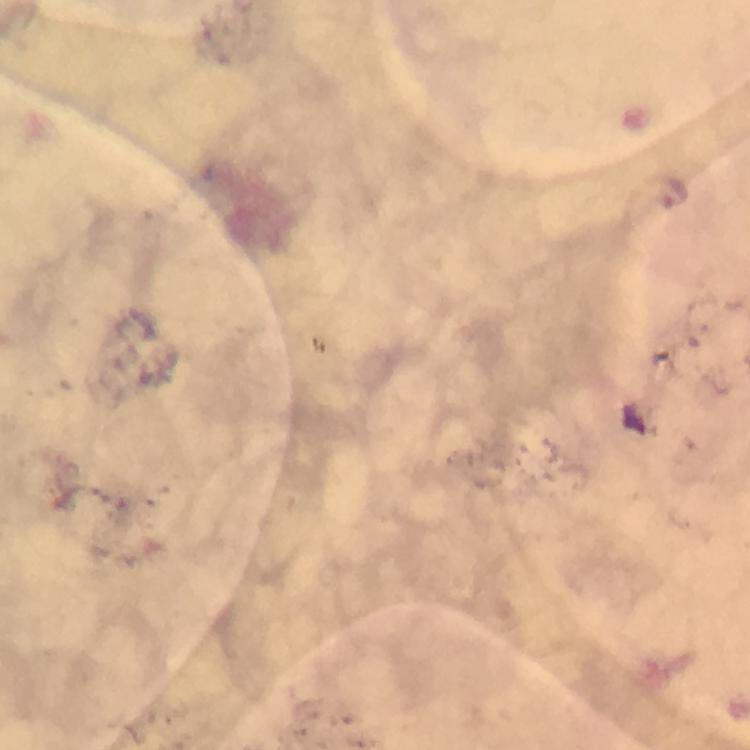

{
  "magnification": "100x",
  "cropped_from": "a single field of view",
  "image_size": "750×750 pixels",
  "immersion_oil": "applied",
  "plasmodium_parasite_locations": "approximate centers as {x, y} in pixels: {672, 192}",
  "preparation": "thick smear",
  "context": "from a diagnostic examination for malaria",
  "capture": "smartphone camera through the microscope",
  "stain": "Giemsa"
}